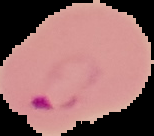 From a thin blood smear. Segmented cell region on a black background. Image is 154×136 pixels. Malaria status: parasitized.